Report the malaria status of this cell.
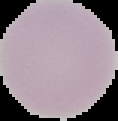
Uninfected.

Summary:
  - Preparation: thin blood smear
  - Image type: segmented cell region on a black background
  - Image size: 118×121 pixels